Identify the cell.
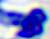

This is a leukocyte.

Summary:
  - Magnification: 400x
  - Modality: micrograph